State which parasite is depicted.
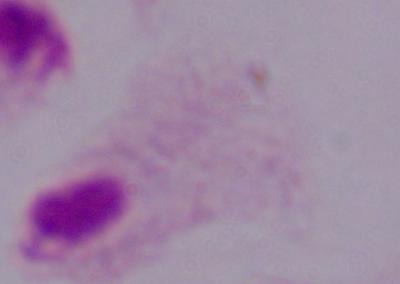
This is a trichomonad.

Summary:
  - Magnification: 1000x
  - Modality: photomicrograph